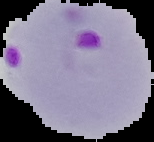 Result: Plasmodium parasites identified. From a thin blood smear. The area outside the segmented cell region is set to black. Image is 154×142 pixels.